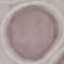

Summary:
  - Result: no malaria parasites seen
  - Stain: Giemsa
  - Image type: automatically extracted cell patch, resized to 64 × 64 pixels
  - Capture: smartphone through the microscope eyepiece
  - Preparation: thin blood smear